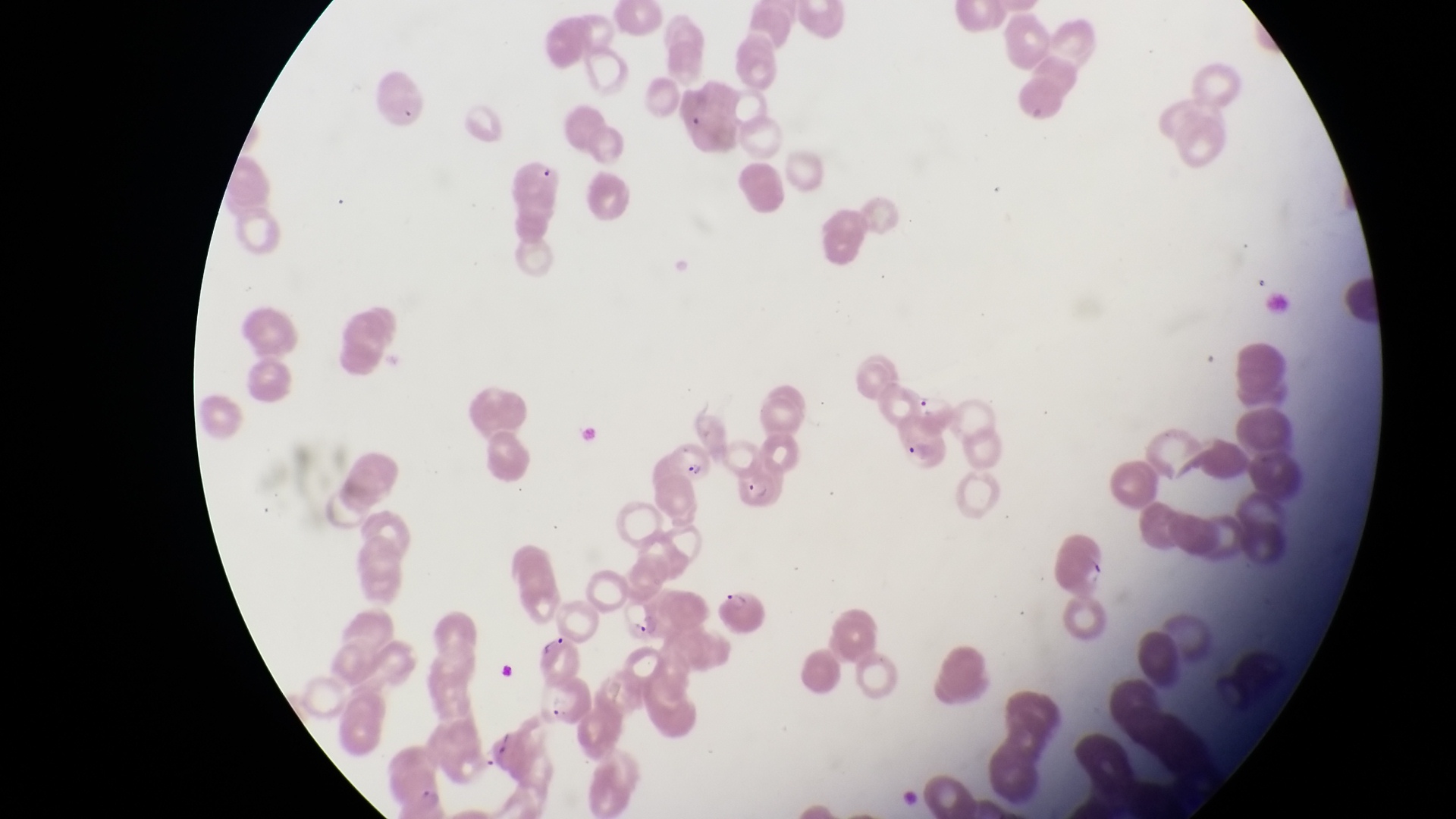

field of view = single
image size = 1456×819 pixels
preparation = thin blood film
capture = smartphone photograph through the eyepiece of an Olympus CX-23 microscope
parasitised red blood cell locations = approximate bounding boxes as [left, top, right, bottom] in pixels: [898, 415, 956, 476], [667, 441, 716, 490], [733, 452, 792, 513], [716, 579, 771, 642], [624, 601, 671, 647], [531, 676, 590, 739]
country = Uganda
magnification = 1000x